Identify the parasite.
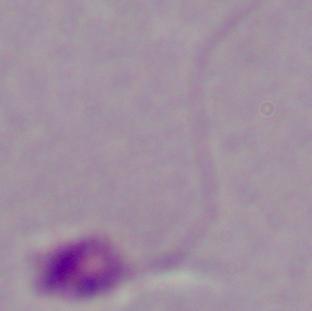
This is Leishmania.

Captured at 1000x magnification. Micrograph.